Outline each blood parasite and name the species.
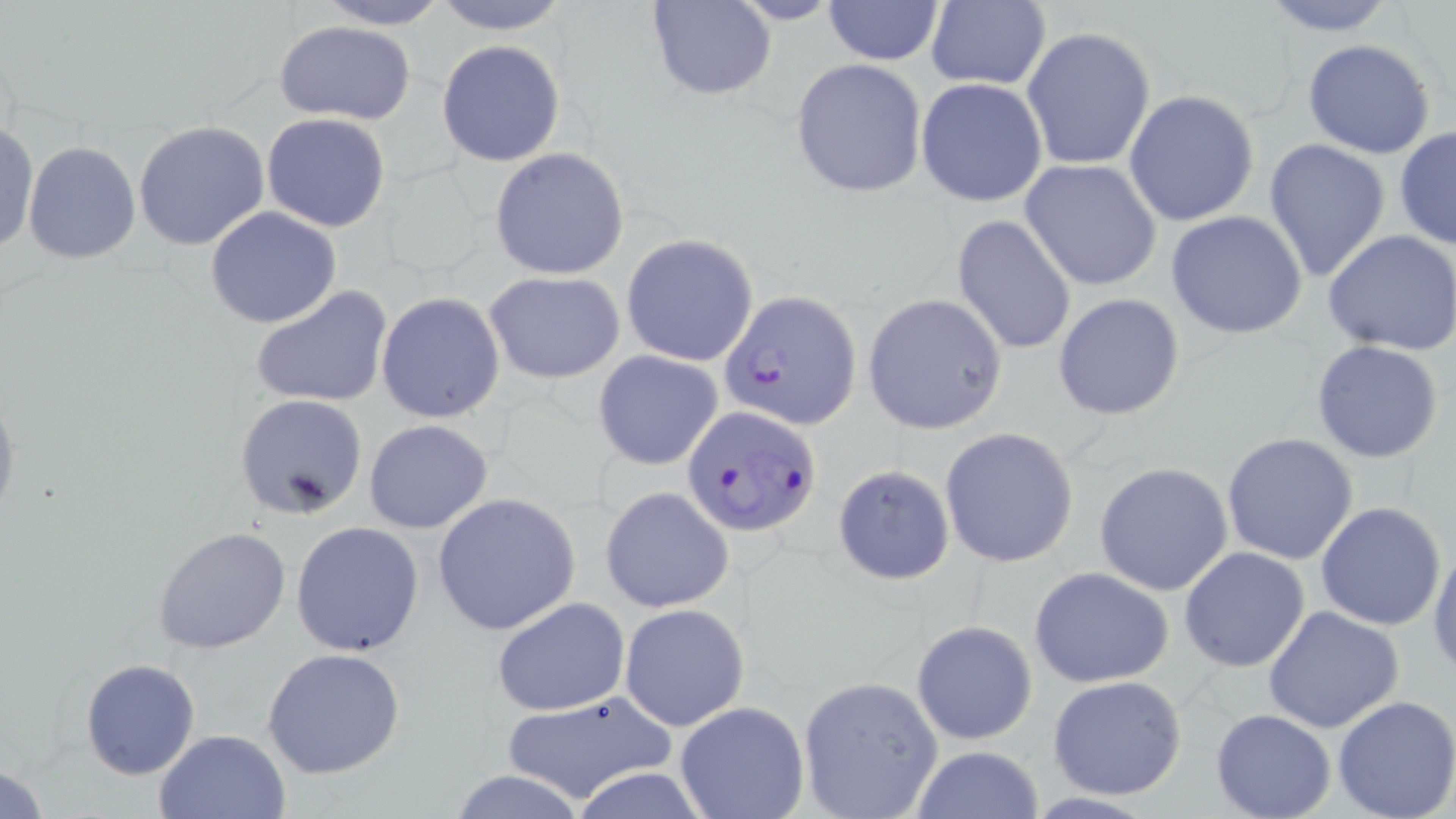

Approximate bounding boxes as named x1/y1/x2/y2 corners in pixels.
Plasmodium falciparum-infected red blood cells: (x1=720, y1=288, x2=862, y2=429), (x1=682, y1=404, x2=819, y2=536).
No Plasmodium ovale, Plasmodium malariae, Plasmodium vivax, Babesia divergens, or Trypanosoma brucei observed.

Summary:
  - Uninfected red blood cell locations: (x1=315, y1=0, x2=451, y2=29), (x1=430, y1=0, x2=570, y2=35), (x1=1259, y1=0, x2=1401, y2=36), (x1=647, y1=1, x2=776, y2=100), (x1=822, y1=1, x2=945, y2=67), (x1=924, y1=1, x2=1051, y2=91), (x1=274, y1=21, x2=417, y2=126), (x1=1021, y1=26, x2=1156, y2=172), (x1=1303, y1=38, x2=1437, y2=159), (x1=436, y1=40, x2=566, y2=167), (x1=790, y1=59, x2=927, y2=199), (x1=916, y1=77, x2=1049, y2=207), (x1=1123, y1=90, x2=1260, y2=227), (x1=261, y1=113, x2=390, y2=233), (x1=0, y1=119, x2=38, y2=257), (x1=133, y1=120, x2=272, y2=250), (x1=1394, y1=126, x2=1456, y2=250), (x1=1263, y1=138, x2=1391, y2=284), (x1=23, y1=140, x2=140, y2=263), (x1=488, y1=147, x2=630, y2=281), (x1=1020, y1=160, x2=1162, y2=289), (x1=205, y1=205, x2=342, y2=329), (x1=1166, y1=211, x2=1310, y2=340), (x1=951, y1=214, x2=1077, y2=357), (x1=1322, y1=228, x2=1456, y2=355), (x1=621, y1=235, x2=760, y2=367), (x1=485, y1=272, x2=624, y2=384), (x1=251, y1=285, x2=393, y2=409), (x1=377, y1=292, x2=505, y2=422), (x1=862, y1=293, x2=1007, y2=432), (x1=1053, y1=293, x2=1186, y2=421), (x1=1310, y1=339, x2=1445, y2=464), (x1=594, y1=350, x2=723, y2=471), (x1=0, y1=382, x2=21, y2=537), (x1=234, y1=394, x2=368, y2=519), (x1=363, y1=418, x2=494, y2=534), (x1=939, y1=427, x2=1079, y2=568), (x1=1221, y1=432, x2=1359, y2=564), (x1=1094, y1=462, x2=1236, y2=597), (x1=832, y1=464, x2=955, y2=585), (x1=599, y1=486, x2=734, y2=612), (x1=432, y1=493, x2=581, y2=635), (x1=1314, y1=501, x2=1447, y2=632), (x1=291, y1=521, x2=423, y2=655), (x1=151, y1=526, x2=291, y2=654), (x1=1429, y1=539, x2=1456, y2=676), (x1=1179, y1=547, x2=1311, y2=671), (x1=1029, y1=566, x2=1175, y2=688), (x1=492, y1=598, x2=630, y2=716), (x1=619, y1=603, x2=749, y2=732), (x1=1263, y1=606, x2=1404, y2=734), (x1=911, y1=619, x2=1039, y2=744), (x1=261, y1=647, x2=407, y2=780), (x1=79, y1=658, x2=201, y2=779), (x1=1048, y1=674, x2=1188, y2=800), (x1=797, y1=675, x2=944, y2=819), (x1=496, y1=690, x2=682, y2=805), (x1=1332, y1=696, x2=1456, y2=819), (x1=674, y1=701, x2=809, y2=819), (x1=1210, y1=709, x2=1336, y2=819), (x1=154, y1=728, x2=291, y2=818), (x1=907, y1=745, x2=1045, y2=819), (x1=0, y1=761, x2=53, y2=818), (x1=447, y1=771, x2=592, y2=819)
  - Slide-level diagnosis: Plasmodium falciparum
  - Modality: optical microscopy
  - Field of view: single
  - Preparation: thin blood film
  - Image size: 1456×819 pixels
  - Stain: May-Grünwald-Giemsa
  - Magnification: 1000x